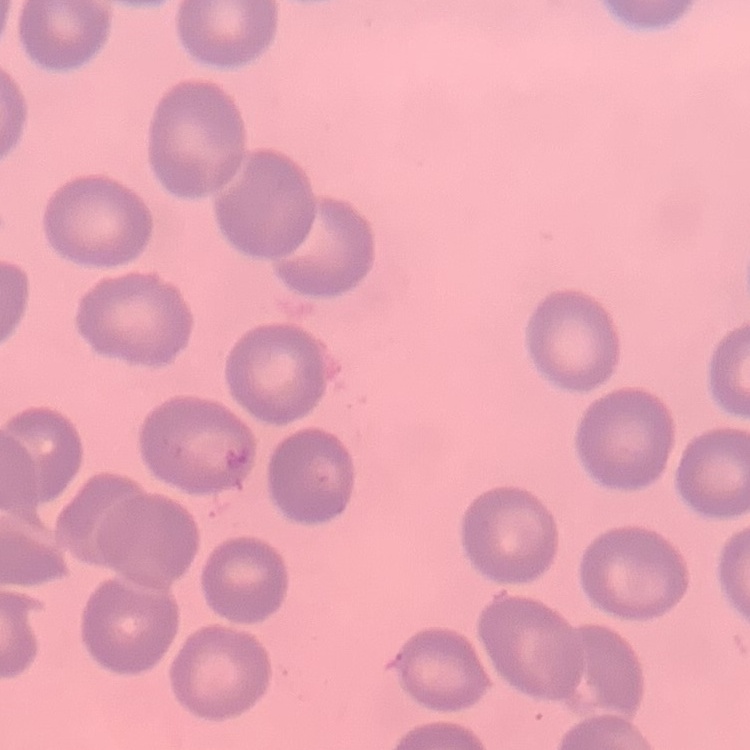

red_blood_cell_morphology: no rouleaux formation
image_type: one tile cut from a larger photomicrograph
stain: Field's or Giemsa
preparation: thin blood smear